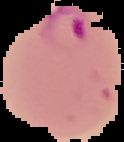

Image is 124×142 pixels. From a thin blood smear. The area outside the segmented cell region is set to black. Result: malaria parasites identified.